Locate leukocytes (white blood cells).
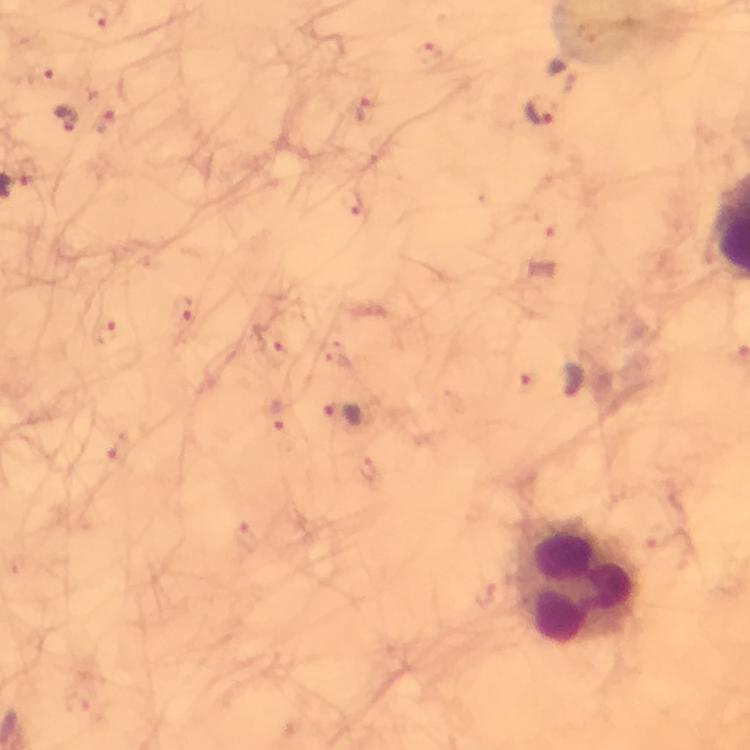

Approximate centers as {x, y} in pixels.
Leukocytes: {583, 580}.

malaria parasite locations = approximate centers as {x, y} in pixels: {99, 17}, {428, 55}, {564, 74}, {367, 111}, {541, 115}, {68, 118}, {106, 124}, {352, 202}, {182, 310}, {108, 333}, {275, 348}, {571, 381}, {526, 383}, {278, 416}, {345, 416}
magnification = 100x
image size = 750×750 pixels
stain = Giemsa
cropped from = one field of view
capture = smartphone mounted on the microscope
context = from a diagnostic examination for malaria
preparation = thick smear
immersion oil = used